Comment on the morphology of the red blood cells.
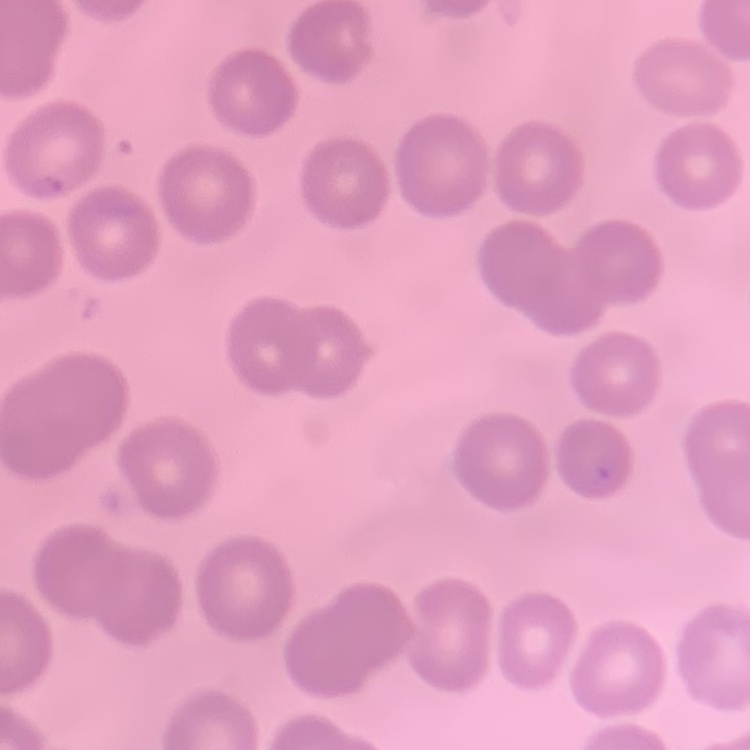
They show no rouleaux formation.

Thin blood smear. One tile cut from a larger photomicrograph. Field's or Giemsa stain.